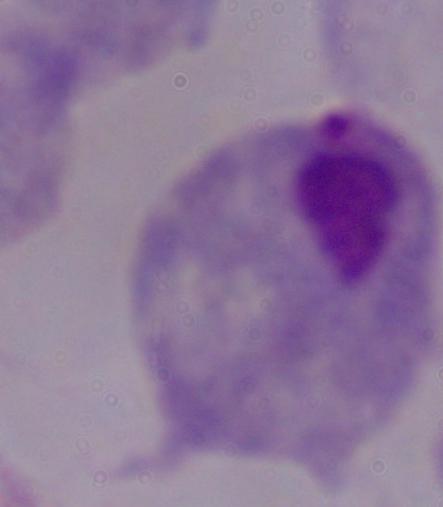

Micrograph. Captured at 1000x magnification. A trichomonad is seen.